Report the malaria status of this cell.
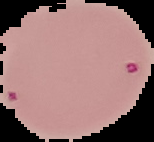
Parasitized.

From a thin blood film. Image is 154×142 pixels. Cell region segmented out of the field of view; the surrounding area is masked to black.